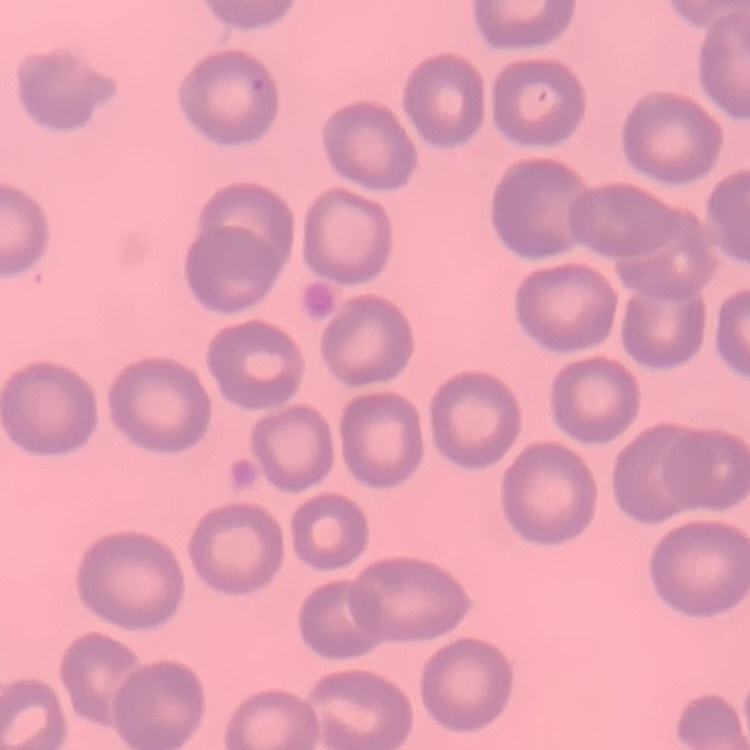

Summary:
  - Erythrocyte morphology: no rouleaux formation
  - Image type: square crop of a larger photomicrograph
  - Preparation: thin blood film
  - Stain: Field's or Giemsa